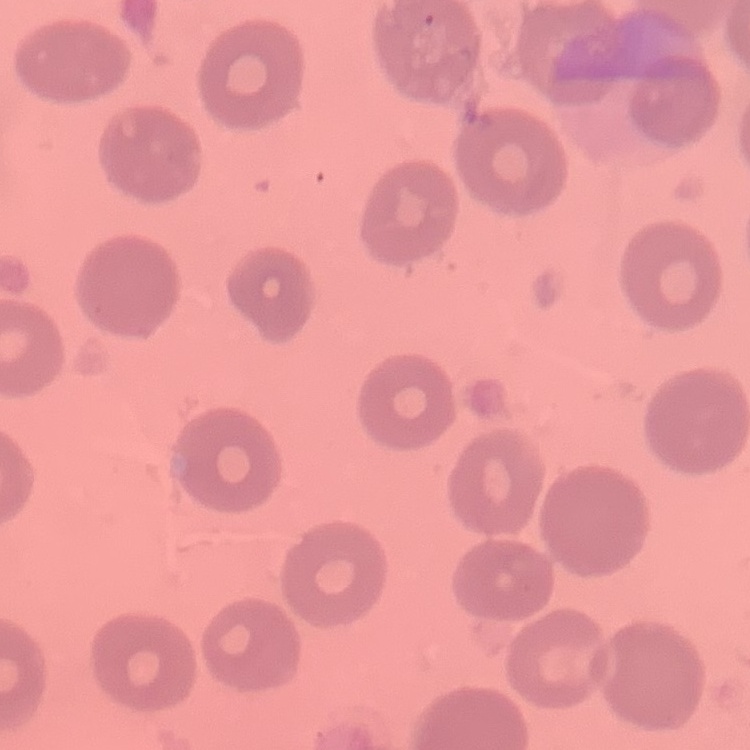
{
  "erythrocyte_morphology": "no rouleaux formation",
  "preparation": "thin peripheral smear",
  "stain": "Field's or Giemsa",
  "image_type": "one tile cut from a larger photomicrograph"
}